Classify this cell by malaria status.
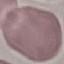

Uninfected.

Summary:
  - Preparation: thin blood smear
  - Image type: cell patch, automatically extracted from a larger field of view and resized to 64 × 64 pixels
  - Stain: Giemsa
  - Capture: smartphone camera at the microscope eyepiece